State which parasite is depicted.
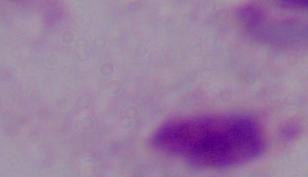
A trichomonad.

Captured at 1000x magnification. Micrograph.